Assess this cell for malaria.
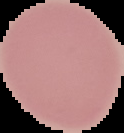
Uninfected.

Image is 124×133 pixels. From a thin blood smear. The area outside the segmented cell region is set to black.